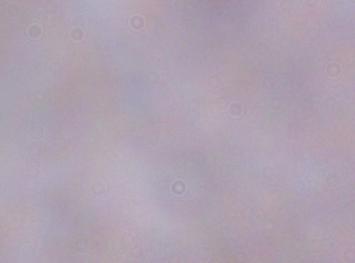
magnification: 1000x
modality: micrograph
identification: trypanosome